Outline each blood parasite and name the species.
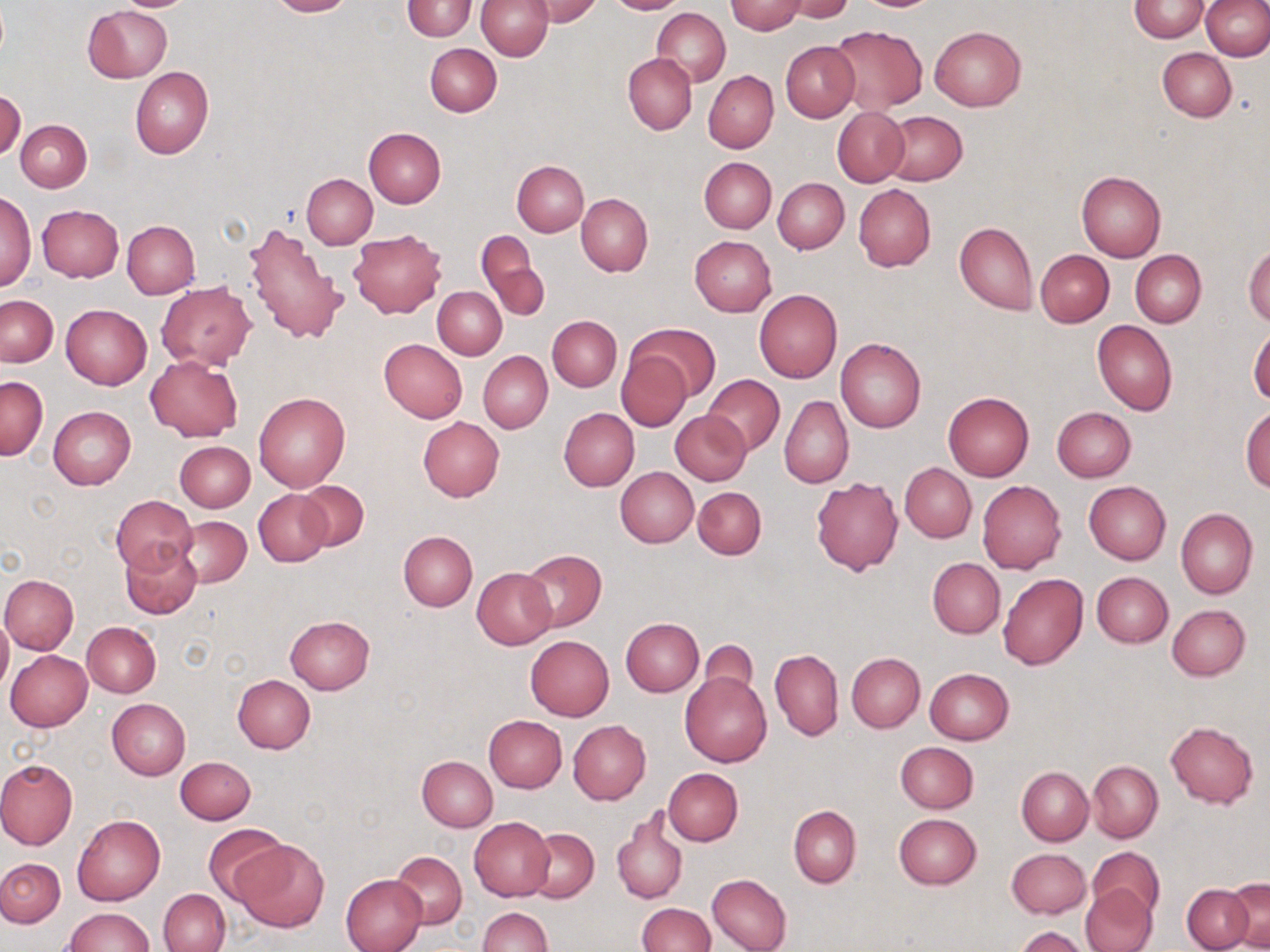

No blood parasites seen.

slide_level_diagnosis: no evidence of blood parasites
magnification: 1000x
modality: light microscopy
uninfected_red_blood_cell_locations: 'approximate bounding boxes as (x1,y1)-(x2,y2) corner pairs in pixels: (267,0)-(354,17), (403,0)-(477,41), (475,0)-(553,60), (528,0)-(601,25), (605,0)-(686,15), (786,0)-(854,22), (1202,0)-(1270,60), (725,1)-(806,35), (1131,1)-(1208,42), (84,5)-(172,82), (652,7)-(731,87), (829,25)-(928,114), (931,26)-(1026,110), (425,42)-(502,117), (782,42)-(859,123), (1157,48)-(1236,121), (623,52)-(697,135), (130,67)-(214,159), (703,71)-(778,153), (0,89)-(25,161), (833,108)-(908,185), (881,111)-(967,185), (16,119)-(91,191), (363,127)-(447,208), (700,157)-(775,233), (512,159)-(589,236), (1076,171)-(1166,261), (302,174)-(377,248), (773,178)-(849,253), (853,183)-(935,272), (1,192)-(35,291), (576,193)-(653,276), (37,205)-(124,282), (243,219)-(348,344), (122,220)-(199,298), (955,222)-(1036,314), (348,230)-(446,318), (476,230)-(546,321), (690,236)-(776,316), (1245,244)-(1270,325), (1036,250)-(1114,326), (1131,250)-(1206,328), (157,281)-(256,370), (433,286)-(506,359), (754,290)-(842,382), (1,296)-(57,365), (61,304)-(151,388), (547,315)-(621,391), (1092,320)-(1177,416), (631,323)-(719,403), (1249,325)-(1270,405), (379,338)-(467,423), (836,338)-(925,433), (615,349)-(694,431), (479,351)-(552,433), (146,356)-(242,442), (703,375)-(785,455), (0,376)-(47,459), (254,392)-(350,491), (943,393)-(1033,480), (780,395)-(853,488), (48,406)-(136,489), (1052,406)-(1136,481), (1241,406)-(1270,493), (559,407)-(639,491), (671,409)-(751,485), (418,416)-(504,501), (174,441)-(255,511), (900,464)-(977,542), (616,467)-(698,547), (811,477)-(903,575), (297,480)-(369,552), (977,481)-(1066,574), (1084,481)-(1171,564), (693,486)-(765,559), (253,489)-(331,567), (111,495)-(198,575), (1176,508)-(1257,600), (174,516)-(252,589), (398,530)-(477,611), (120,542)-(201,619), (519,548)-(607,631), (927,558)-(1004,638), (471,567)-(557,649), (1091,571)-(1173,647), (1,574)-(78,653), (998,574)-(1089,670), (1168,604)-(1250,680), (0,611)-(12,693), (284,616)-(374,694), (621,618)-(704,696), (81,621)-(161,697), (526,635)-(614,720), (694,639)-(762,702), (769,649)-(843,740), (5,650)-(93,732), (846,653)-(925,732), (924,668)-(1015,745), (680,671)-(771,767), (232,674)-(314,753), (106,698)-(190,780), (484,715)-(567,792), (567,720)-(650,805), (1165,721)-(1258,809), (895,741)-(979,813), (175,755)-(256,823), (417,755)-(497,831), (0,758)-(77,849), (1087,761)-(1162,842), (1017,766)-(1093,844), (663,767)-(743,845), (789,806)-(861,887), (612,808)-(688,905), (72,814)-(165,906), (894,814)-(982,890), (468,817)-(554,902), (201,823)-(290,903), (526,829)-(599,903), (233,839)-(329,933), (1089,846)-(1161,915), (1006,848)-(1091,919), (392,852)-(466,928), (0,857)-(64,927), (341,874)-(428,952), (707,874)-(792,952), (1227,879)-(1270,949), (1182,883)-(1253,951), (1080,885)-(1156,952), (159,888)-(230,952), (637,903)-(714,952), (61,907)-(153,952), (477,907)-(551,952), (1015,926)-(1091,952)'
stain: May-Grünwald-Giemsa
image_size: 1270×952 pixels
preparation: thin blood smear
field_of_view: one of a larger specimen